State which parasite is depicted.
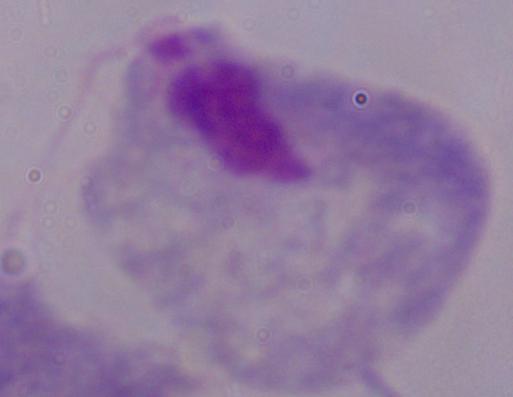

A trichomonad.

Summary:
  - Modality: photomicrograph
  - Magnification: 1000x